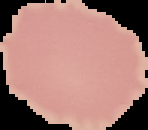

Malaria status: uninfected. Cell region segmented out of the field of view; the surrounding area is masked to black. Image is 148×130 pixels. From a thin blood smear.